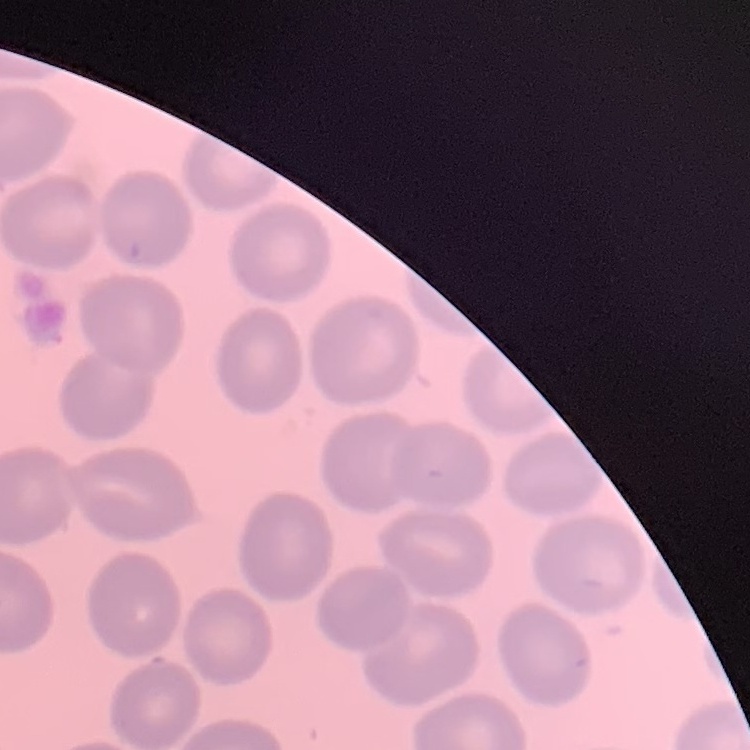

erythrocyte morphology = no rouleaux formation
preparation = thin blood film
image type = one tile cut from a larger photomicrograph
stain = Field's or Giemsa